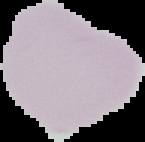 Image is 145×142 pixels. Segmented cell region on a black background. Malaria status: uninfected. From a thin blood smear.